Classify this cell by malaria status.
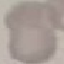

It is uninfected.

stain = Giemsa
image type = automatically extracted cell patch, resized to 64 × 64 pixels
preparation = thin blood smear
capture = smartphone camera at the microscope eyepiece